Comment on the morphology of the red blood cells.
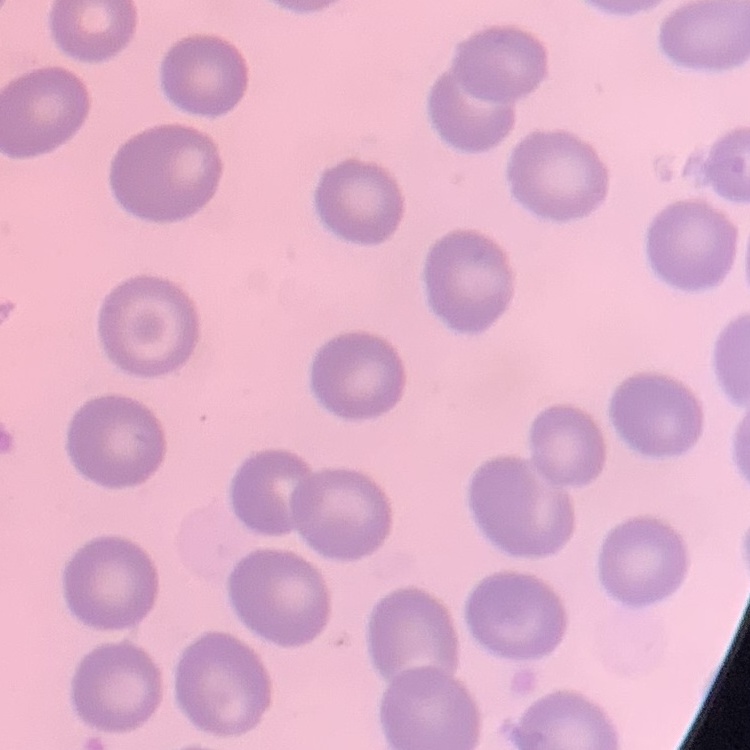
They show no rouleaux formation.

Summary:
  - Stain: Field's or Giemsa
  - Preparation: thin blood smear
  - Image type: square crop of a larger photomicrograph